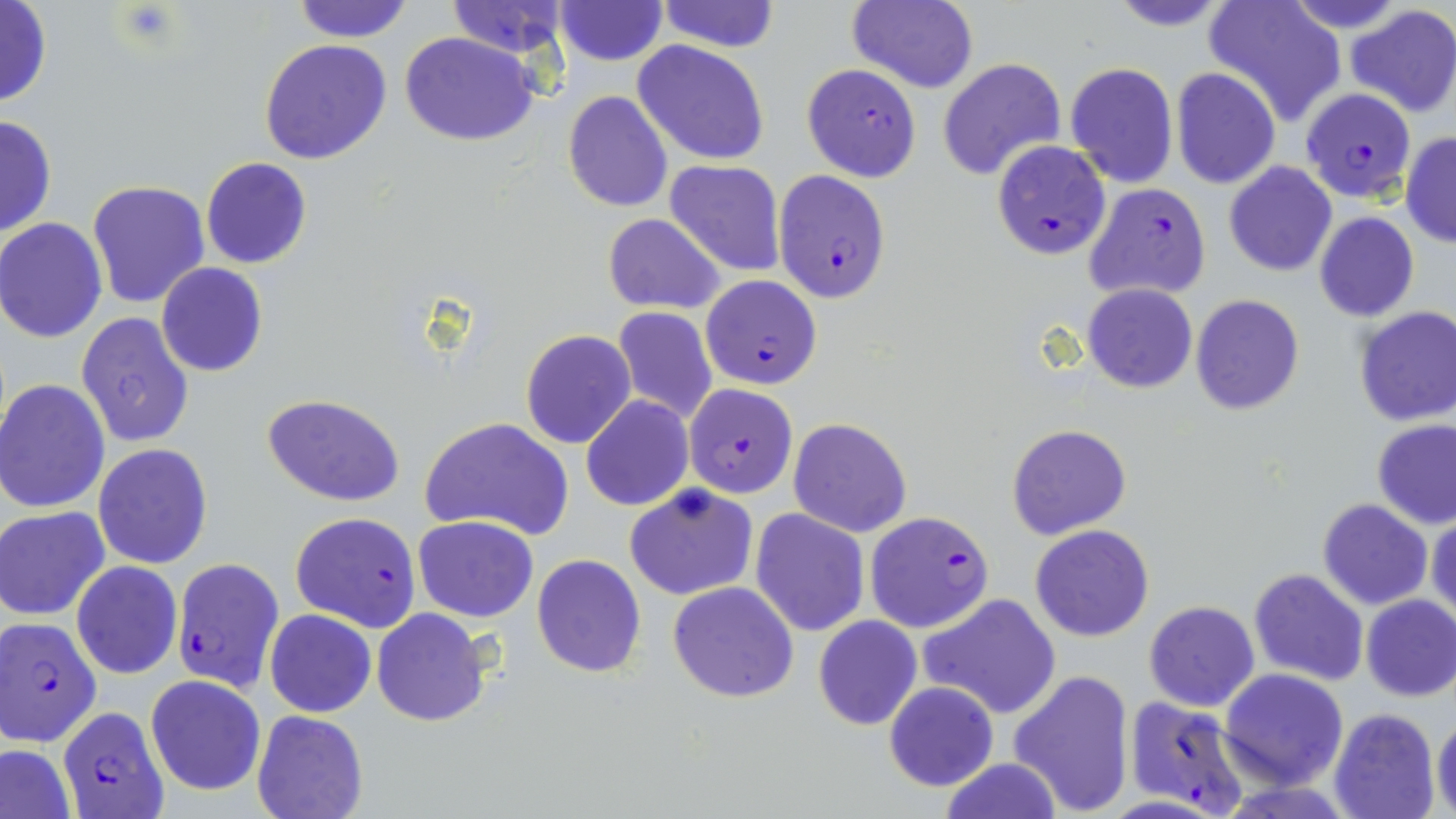 Approximate bounding boxes as (x1,y1)-(x2,y2) corner pairs in pixels. Uninfected red blood cell locations: (656,0)-(781,53), (847,0)-(980,94), (1102,0)-(1239,31), (1205,0)-(1345,124), (1279,0)-(1411,35), (0,1)-(51,108), (289,1)-(416,42), (445,1)-(574,60), (554,1)-(666,67), (1346,5)-(1456,119), (400,31)-(541,146), (258,40)-(392,165), (631,41)-(771,167), (938,57)-(1066,180), (1066,63)-(1179,188), (1170,68)-(1281,190), (562,90)-(673,213), (0,114)-(56,240), (1400,131)-(1456,248), (201,157)-(312,269), (664,160)-(784,276), (1224,160)-(1338,276), (85,179)-(211,309), (1315,211)-(1420,320), (603,213)-(726,313), (0,217)-(108,343), (156,263)-(269,378), (1082,284)-(1197,393), (1190,294)-(1304,414), (612,307)-(718,426), (1353,307)-(1456,427), (76,311)-(194,448), (520,329)-(636,448), (0,380)-(110,513), (262,393)-(406,507), (580,395)-(696,511), (419,417)-(575,540), (787,417)-(912,537), (1372,418)-(1456,529), (1006,423)-(1133,540), (92,444)-(212,568), (625,483)-(760,601), (1317,499)-(1432,609), (1,505)-(112,620), (750,509)-(868,635), (1428,509)-(1456,625), (412,516)-(541,621), (1030,525)-(1155,642), (531,554)-(647,677), (71,561)-(184,679), (1249,568)-(1370,686), (667,582)-(799,701), (921,595)-(1060,719), (1360,595)-(1456,702), (1143,601)-(1260,712), (371,608)-(489,728), (265,610)-(376,718), (813,616)-(922,731), (1219,668)-(1348,789), (1009,669)-(1135,816), (145,675)-(267,797), (883,681)-(999,791), (1329,707)-(1440,819), (251,710)-(369,819), (1433,713)-(1456,819), (0,744)-(78,819), (939,757)-(1062,819). Plasmodium falciparum-infected red blood cell locations: (801,63)-(921,182), (1300,89)-(1414,202), (991,141)-(1111,259), (772,169)-(891,301), (1085,181)-(1210,301), (700,274)-(822,389), (684,383)-(798,498), (290,510)-(422,631), (866,510)-(991,632), (171,557)-(284,692), (2,617)-(102,746), (1124,696)-(1253,817), (56,707)-(168,819). Platelet locations: (116,3)-(179,48). Slide-level diagnosis: Plasmodium falciparum. Thin blood film. May-Grünwald-Giemsa-stained preparation. 1000x magnification. Light microscopy. One field of a larger specimen. Image is 1456×819 pixels.